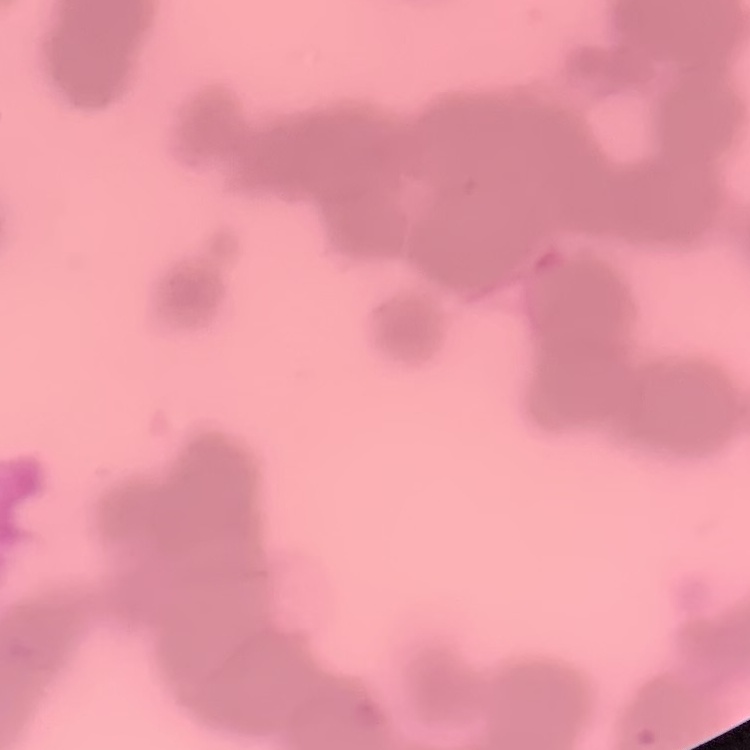

erythrocyte morphology = rouleaux formation
preparation = thin blood smear
image type = square crop of a larger photomicrograph
stain = Field's or Giemsa